Report the malaria status of this cell.
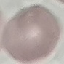

Uninfected.

Summary:
  - Capture: smartphone through the microscope eyepiece
  - Stain: Giemsa
  - Image type: automatically extracted cell patch, resized to 64 × 64 pixels
  - Preparation: thin blood film